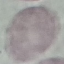

malaria status = uninfected
image type = automatically extracted cell patch, resized to 64 × 64 pixels
capture = smartphone through the microscope eyepiece
stain = Giemsa
preparation = thin blood smear